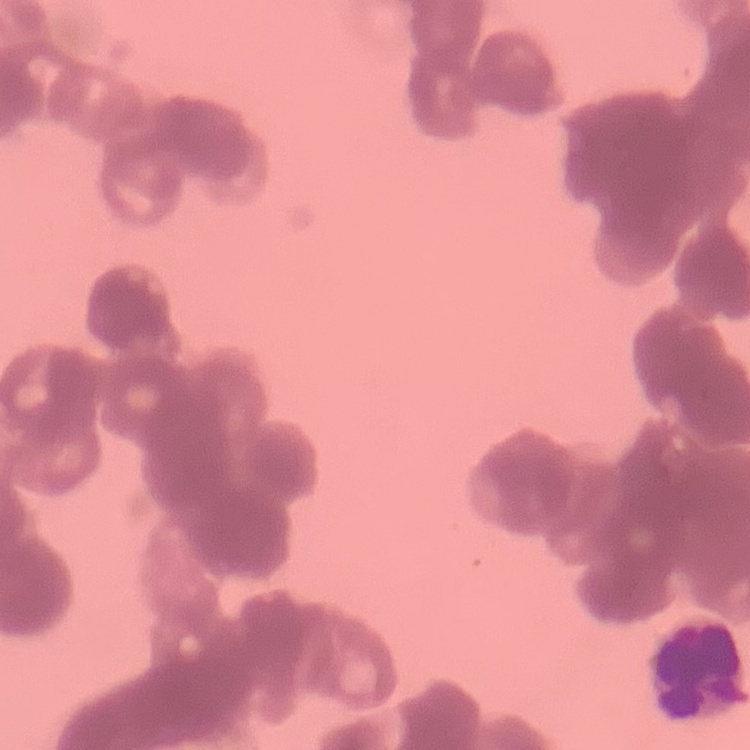
red blood cell morphology = rouleaux formation
stain = Field's or Giemsa
image type = one tile cut from a larger photomicrograph
preparation = thin peripheral smear